Locate every blood parasite and identify its species.
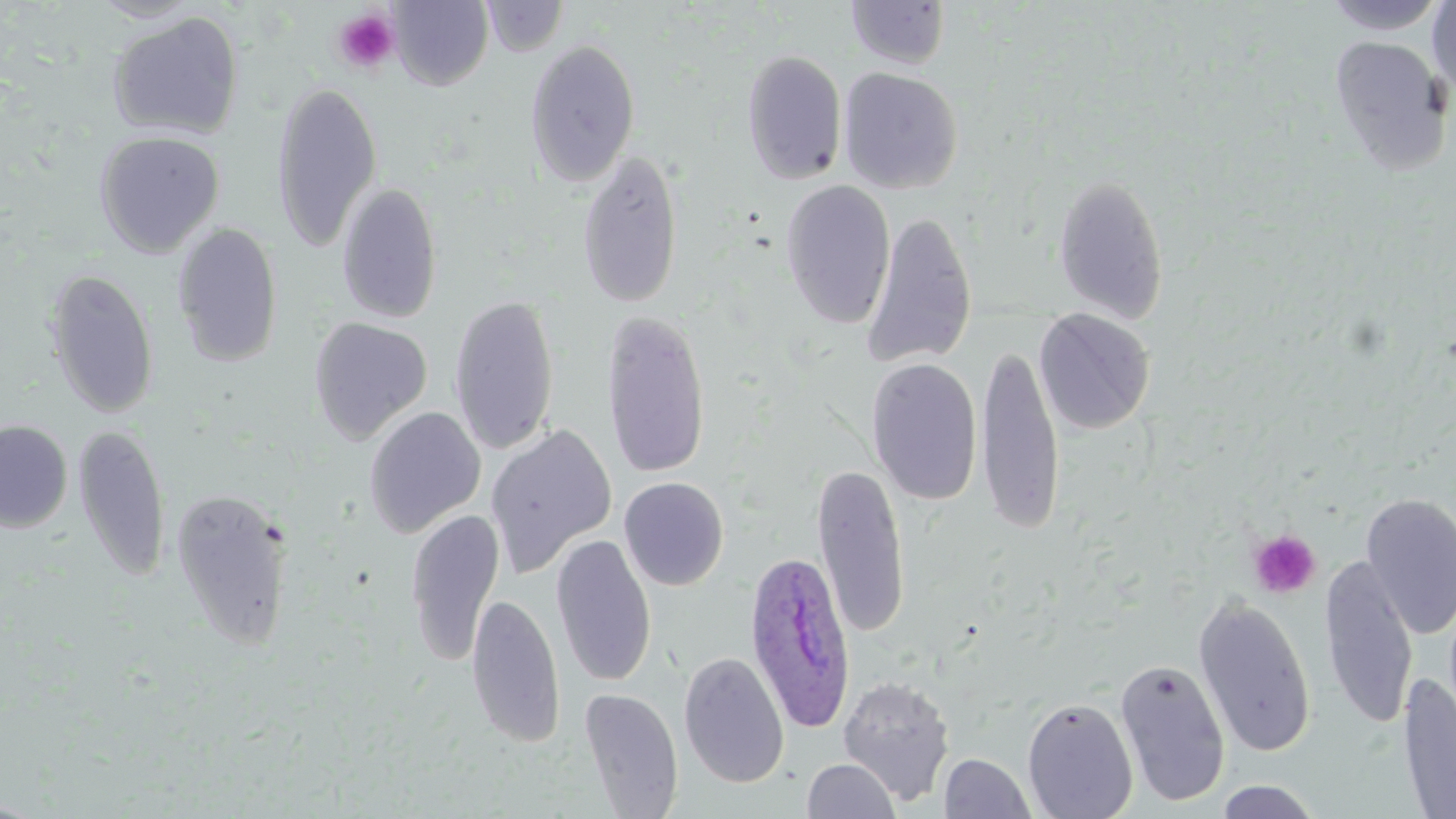
Approximate bounding boxes as (x1,y1)-(x2,y2) corner pairs in pixels.
Plasmodium ovale-infected red blood cells: (743,548)-(856,733).
No Plasmodium falciparum, Plasmodium malariae, Plasmodium vivax, Babesia divergens, or Trypanosoma brucei observed.

Platelet locations: (331,8)-(401,75), (1248,529)-(1321,598). Uninfected red blood cell locations: (389,0)-(493,90), (482,0)-(568,57), (1323,0)-(1448,34), (1427,0)-(1456,99), (845,1)-(951,70), (108,11)-(244,141), (1328,35)-(1452,177), (525,38)-(641,189), (741,49)-(848,185), (838,67)-(963,194), (271,80)-(383,254), (93,130)-(225,257), (576,150)-(684,310), (1053,174)-(1169,326), (780,180)-(896,330), (337,182)-(443,324), (860,211)-(978,370), (171,223)-(284,367), (44,268)-(160,419), (448,293)-(560,456), (601,308)-(711,481), (1034,308)-(1155,434), (308,316)-(433,445), (975,342)-(1065,536), (865,358)-(984,506), (363,406)-(487,538), (0,420)-(73,533), (73,422)-(170,582), (485,424)-(617,578), (812,462)-(911,640), (619,476)-(729,591), (169,487)-(294,650), (1359,493)-(1456,640), (405,508)-(505,666), (551,534)-(657,687), (1320,557)-(1419,730), (466,592)-(565,749), (1192,595)-(1317,758), (678,651)-(790,789), (1115,659)-(1230,807), (1399,673)-(1456,819), (837,676)-(956,805), (578,688)-(684,818), (1022,698)-(1138,819), (939,753)-(1036,818), (801,758)-(901,818), (1214,779)-(1322,818). Slide-level diagnosis: Plasmodium ovale. Thin blood smear. Single field of view. 1000x magnification. May-Grünwald-Giemsa stain. Light microscopy. Image is 1456×819 pixels.